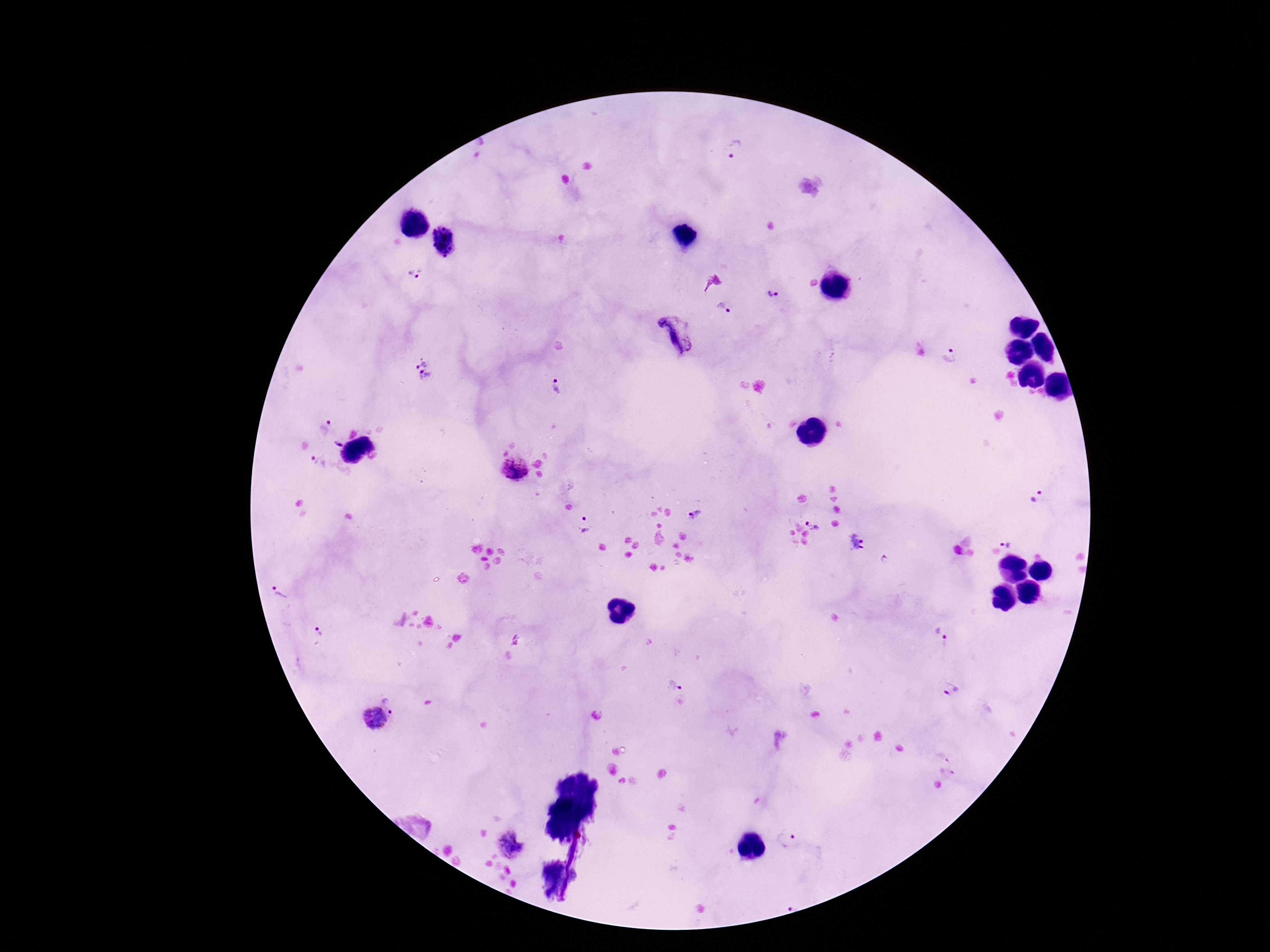 Approximate object centers, in pixels from the top-left corner. Plasmodium parasite locations: (x=738, y=149), (x=415, y=271), (x=774, y=292), (x=723, y=309), (x=674, y=336), (x=951, y=353), (x=424, y=370), (x=557, y=387), (x=324, y=427), (x=337, y=444), (x=318, y=462), (x=513, y=469), (x=1038, y=496), (x=692, y=517), (x=814, y=523), (x=585, y=525), (x=857, y=544), (x=1008, y=544), (x=280, y=592), (x=318, y=631), (x=941, y=636), (x=671, y=686), (x=951, y=690), (x=395, y=701), (x=374, y=720), (x=786, y=840), (x=511, y=844). 100x magnification. Giemsa-stained preparation. Thick blood smear. One field from this slide. Photographed through the microscope eyepiece with a smartphone camera. Patient malaria status: positive. Image is 1270×952 pixels.